Locate and identify every blood parasite.
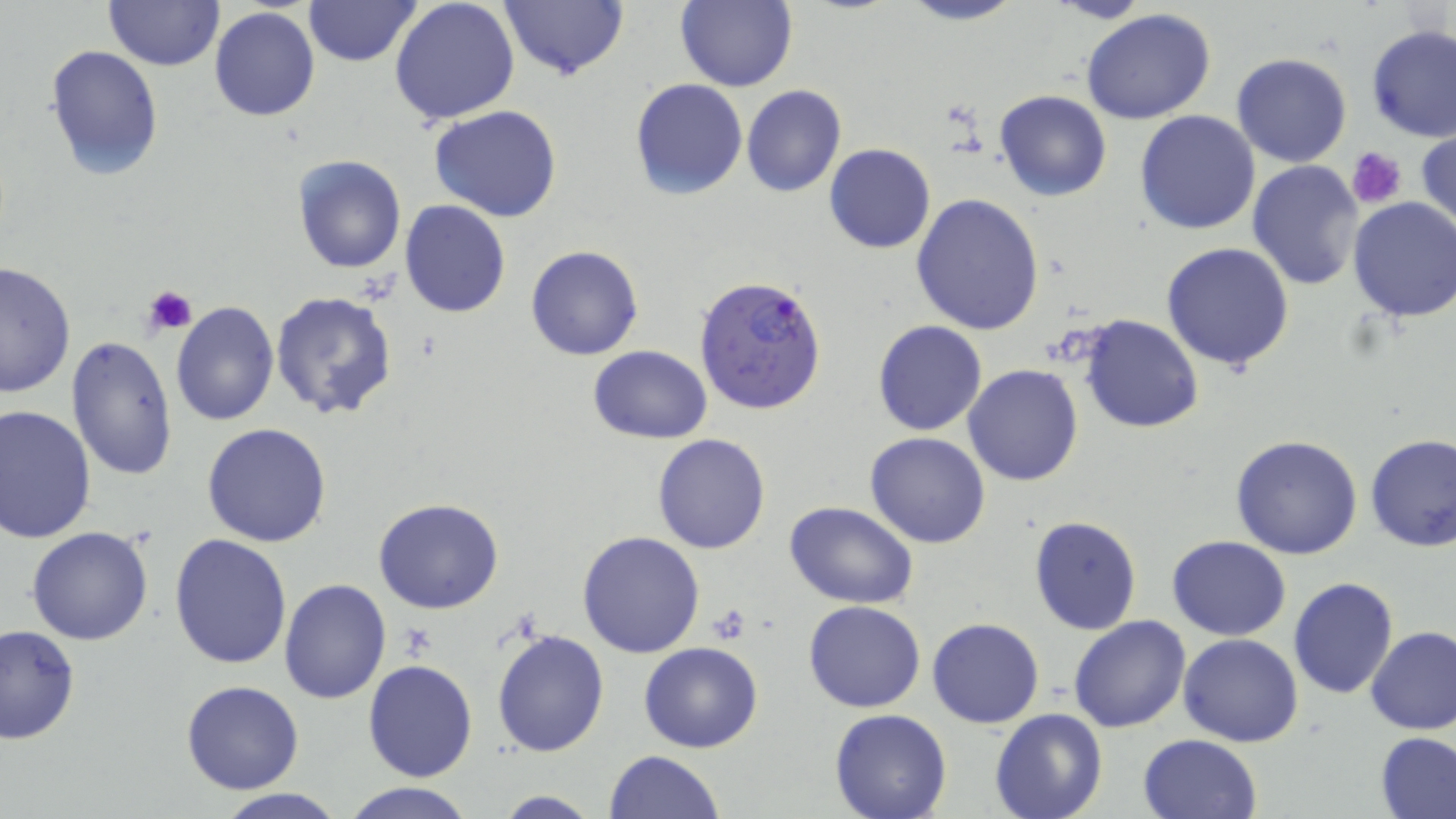

Approximate bounding boxes as named x1/y1/x2/y2 corners in pixels.
Plasmodium falciparum-infected red blood cells: (x1=694, y1=274, x2=829, y2=416).
No Plasmodium ovale, Plasmodium malariae, Plasmodium vivax, Babesia divergens, or Trypanosoma brucei observed.

Summary:
  - Uninfected red blood cell locations: (x1=104, y1=0, x2=222, y2=70), (x1=303, y1=0, x2=420, y2=67), (x1=389, y1=0, x2=521, y2=128), (x1=501, y1=0, x2=627, y2=81), (x1=677, y1=0, x2=798, y2=92), (x1=898, y1=0, x2=1027, y2=25), (x1=209, y1=8, x2=320, y2=123), (x1=1083, y1=9, x2=1216, y2=125), (x1=1367, y1=26, x2=1456, y2=145), (x1=44, y1=44, x2=163, y2=180), (x1=1231, y1=54, x2=1353, y2=168), (x1=629, y1=78, x2=748, y2=200), (x1=742, y1=86, x2=847, y2=198), (x1=994, y1=90, x2=1111, y2=203), (x1=429, y1=105, x2=564, y2=222), (x1=1135, y1=110, x2=1261, y2=234), (x1=1415, y1=123, x2=1456, y2=240), (x1=824, y1=143, x2=936, y2=253), (x1=292, y1=154, x2=407, y2=274), (x1=1246, y1=159, x2=1363, y2=290), (x1=910, y1=192, x2=1045, y2=336), (x1=1346, y1=198, x2=1456, y2=323), (x1=398, y1=201, x2=511, y2=318), (x1=1161, y1=242, x2=1295, y2=372), (x1=524, y1=243, x2=644, y2=360), (x1=0, y1=259, x2=76, y2=399), (x1=271, y1=291, x2=400, y2=421), (x1=170, y1=302, x2=279, y2=427), (x1=1077, y1=314, x2=1205, y2=435), (x1=872, y1=320, x2=988, y2=436), (x1=66, y1=336, x2=177, y2=483), (x1=588, y1=346, x2=712, y2=443), (x1=964, y1=364, x2=1083, y2=485), (x1=0, y1=404, x2=98, y2=544), (x1=202, y1=423, x2=332, y2=547), (x1=865, y1=432, x2=992, y2=548), (x1=652, y1=433, x2=772, y2=554), (x1=1364, y1=433, x2=1456, y2=551), (x1=1231, y1=434, x2=1364, y2=559), (x1=374, y1=496, x2=504, y2=614), (x1=785, y1=501, x2=917, y2=607), (x1=1028, y1=515, x2=1143, y2=636), (x1=27, y1=527, x2=154, y2=646), (x1=576, y1=531, x2=704, y2=658), (x1=169, y1=533, x2=292, y2=671), (x1=1168, y1=535, x2=1290, y2=639), (x1=1288, y1=576, x2=1397, y2=700), (x1=279, y1=579, x2=390, y2=703), (x1=804, y1=600, x2=926, y2=712), (x1=1068, y1=615, x2=1191, y2=733), (x1=927, y1=618, x2=1044, y2=729), (x1=0, y1=625, x2=80, y2=745), (x1=1365, y1=625, x2=1456, y2=735), (x1=492, y1=627, x2=610, y2=758), (x1=1178, y1=634, x2=1304, y2=747), (x1=639, y1=641, x2=763, y2=752), (x1=362, y1=659, x2=478, y2=783), (x1=180, y1=680, x2=305, y2=794), (x1=990, y1=709, x2=1108, y2=819), (x1=829, y1=710, x2=953, y2=819), (x1=1137, y1=732, x2=1262, y2=819), (x1=1376, y1=733, x2=1456, y2=818), (x1=605, y1=750, x2=725, y2=819), (x1=339, y1=782, x2=480, y2=819), (x1=210, y1=790, x2=352, y2=819), (x1=490, y1=791, x2=602, y2=818)
  - Platelet locations: (x1=1346, y1=146, x2=1408, y2=208), (x1=144, y1=286, x2=196, y2=335), (x1=709, y1=605, x2=753, y2=645), (x1=398, y1=624, x2=437, y2=661)
  - Slide-level diagnosis: Plasmodium falciparum
  - Field of view: one of a larger specimen
  - Magnification: 1000x
  - Stain: May-Grünwald-Giemsa
  - Image size: 1456×819 pixels
  - Modality: optical microscopy
  - Preparation: thin blood film